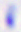

Summary:
  - Identification: Toxoplasma gondii
  - Modality: photomicrograph
  - Magnification: 400x